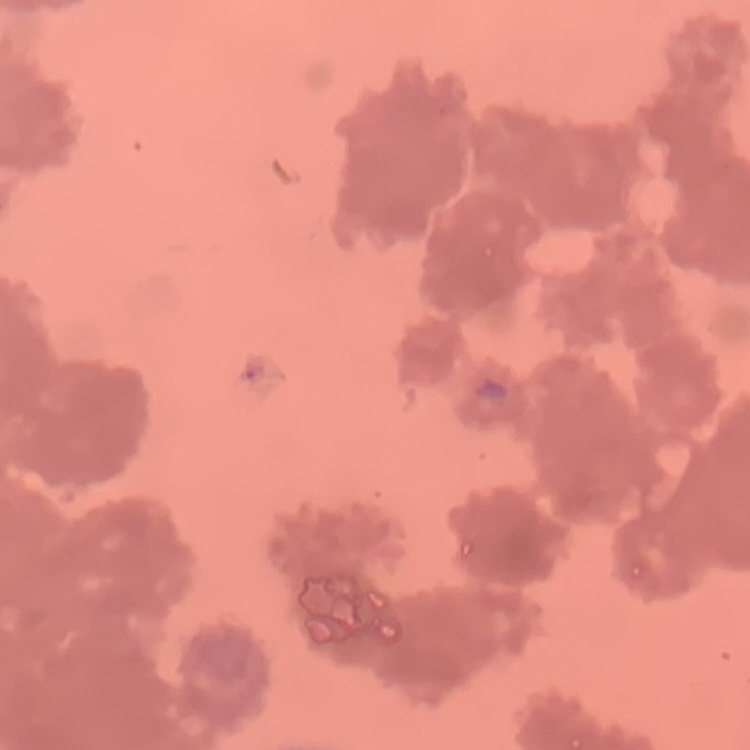
{
  "erythrocyte_morphology": "rouleaux formation",
  "stain": "Field's or Giemsa",
  "preparation": "thin blood smear",
  "image_type": "square crop of a larger photomicrograph"
}